Locate every blood parasite and identify its species.
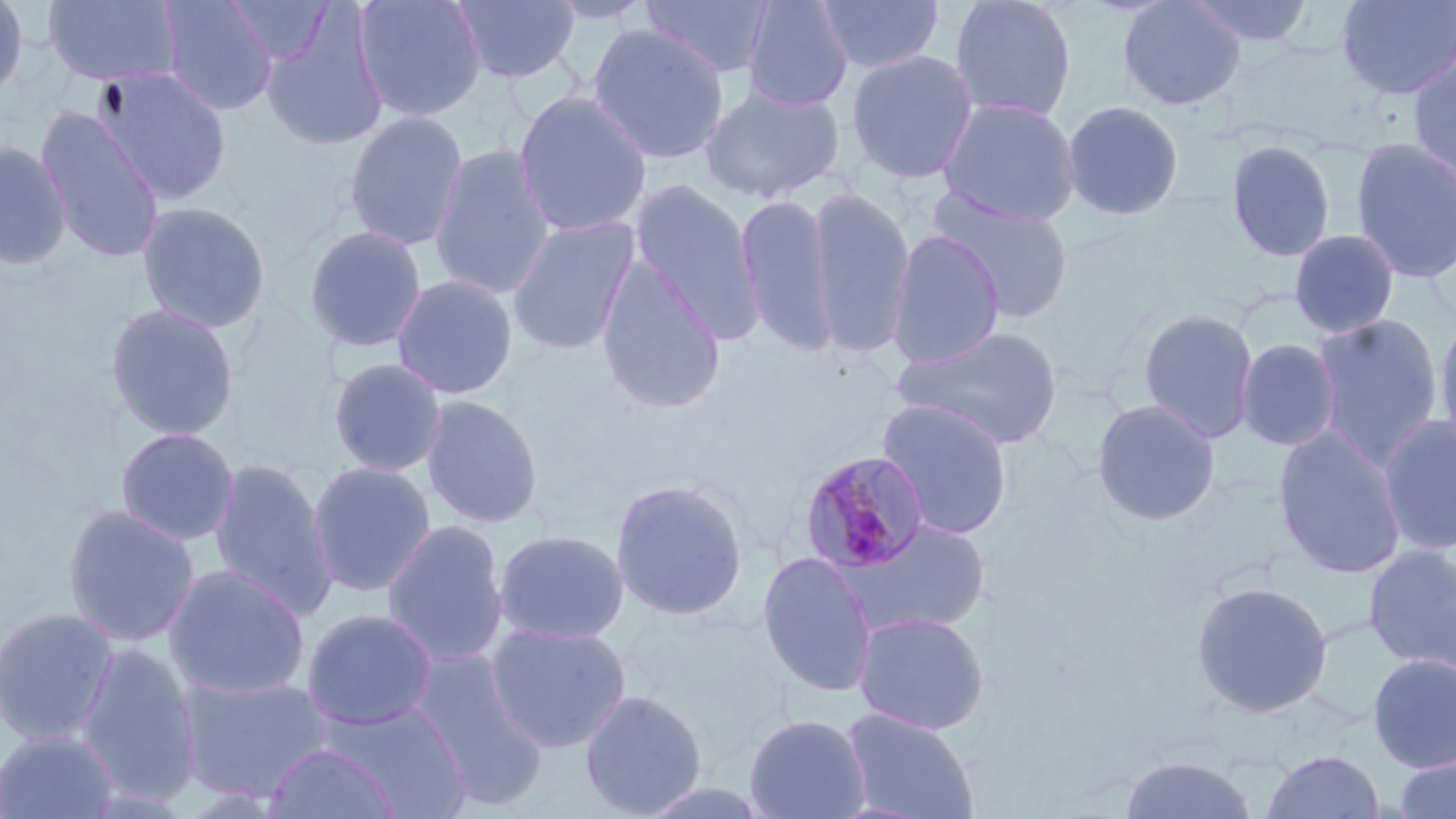
Approximate bounding boxes as (x1, y1, x2, y2) in pixels.
Plasmodium malariae-infected red blood cells: (798, 450, 932, 574).
No Plasmodium falciparum, Plasmodium ovale, Plasmodium vivax, Babesia divergens, or Trypanosoma brucei observed.

Uninfected red blood cell locations: (0, 0, 29, 102), (41, 0, 183, 88), (158, 0, 279, 116), (223, 0, 336, 65), (354, 0, 486, 122), (452, 0, 581, 85), (542, 0, 658, 25), (640, 0, 775, 80), (814, 0, 945, 74), (948, 0, 1078, 123), (1117, 0, 1247, 111), (1185, 0, 1315, 48), (1335, 0, 1456, 100), (740, 1, 855, 112), (261, 11, 389, 152), (587, 24, 730, 165), (845, 49, 979, 184), (1406, 52, 1456, 191), (93, 67, 232, 204), (699, 82, 845, 204), (513, 90, 652, 237), (937, 96, 1081, 226), (1061, 99, 1185, 221), (34, 106, 166, 263), (343, 110, 469, 251), (1350, 137, 1456, 284), (0, 139, 73, 269), (1225, 139, 1336, 263), (428, 143, 556, 300), (629, 177, 765, 342), (807, 184, 916, 359), (928, 188, 1076, 324), (734, 190, 838, 357), (136, 201, 271, 334), (507, 215, 640, 355), (304, 225, 428, 354), (886, 229, 1005, 369), (1288, 229, 1400, 339), (596, 258, 726, 415), (392, 273, 518, 399), (105, 302, 240, 442), (1136, 306, 1260, 444), (1432, 311, 1456, 456), (1309, 313, 1444, 470), (892, 324, 1065, 450), (1236, 338, 1341, 452), (327, 357, 446, 477), (420, 394, 543, 529), (876, 399, 1014, 540), (1091, 399, 1221, 527), (1377, 415, 1456, 556), (115, 427, 240, 546), (1272, 427, 1408, 579), (208, 457, 339, 622), (307, 460, 436, 597), (609, 479, 749, 621), (62, 505, 200, 647), (382, 519, 509, 666), (836, 519, 991, 638), (493, 528, 630, 645), (1363, 544, 1456, 673), (755, 551, 879, 698), (163, 565, 311, 701), (1190, 580, 1333, 719), (0, 606, 120, 746), (301, 608, 438, 731), (852, 610, 990, 735), (484, 621, 632, 754), (76, 643, 203, 808), (409, 650, 549, 810), (1367, 652, 1456, 772), (177, 673, 334, 803), (579, 688, 707, 818), (323, 700, 471, 817), (841, 708, 980, 819), (744, 713, 871, 819), (0, 729, 120, 818), (262, 742, 401, 819), (1260, 749, 1386, 819), (1118, 755, 1260, 818), (1391, 755, 1456, 819). Slide-level diagnosis: Plasmodium malariae. Image is 1456×819 pixels. One field of a larger specimen. Optical microscopy. 1000x magnification. Thin blood film. May-Grünwald-Giemsa-stained preparation.